Name the parasite shown.
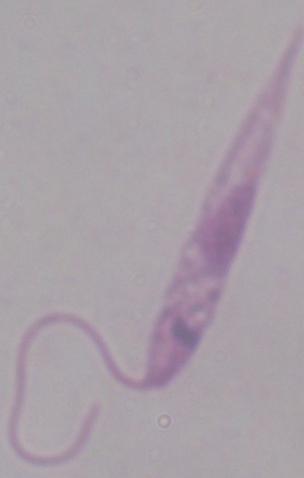

Leishmania.

Photomicrograph. Captured at 1000x magnification.